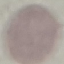

malaria status = uninfected
preparation = thin smear
capture = smartphone camera at the microscope eyepiece
image type = automatically extracted cell patch, resized to 64 × 64 pixels
stain = Giemsa